Assess the morphology of the erythrocytes.
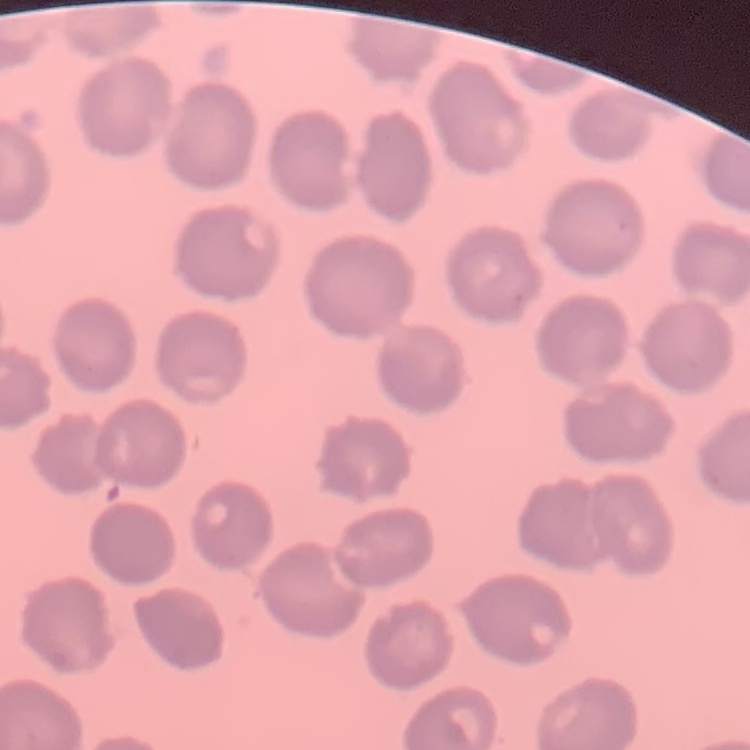
No rouleaux formation.

Summary:
  - Preparation: thin peripheral smear
  - Image type: one tile cut from a larger photomicrograph
  - Stain: Field's or Giemsa